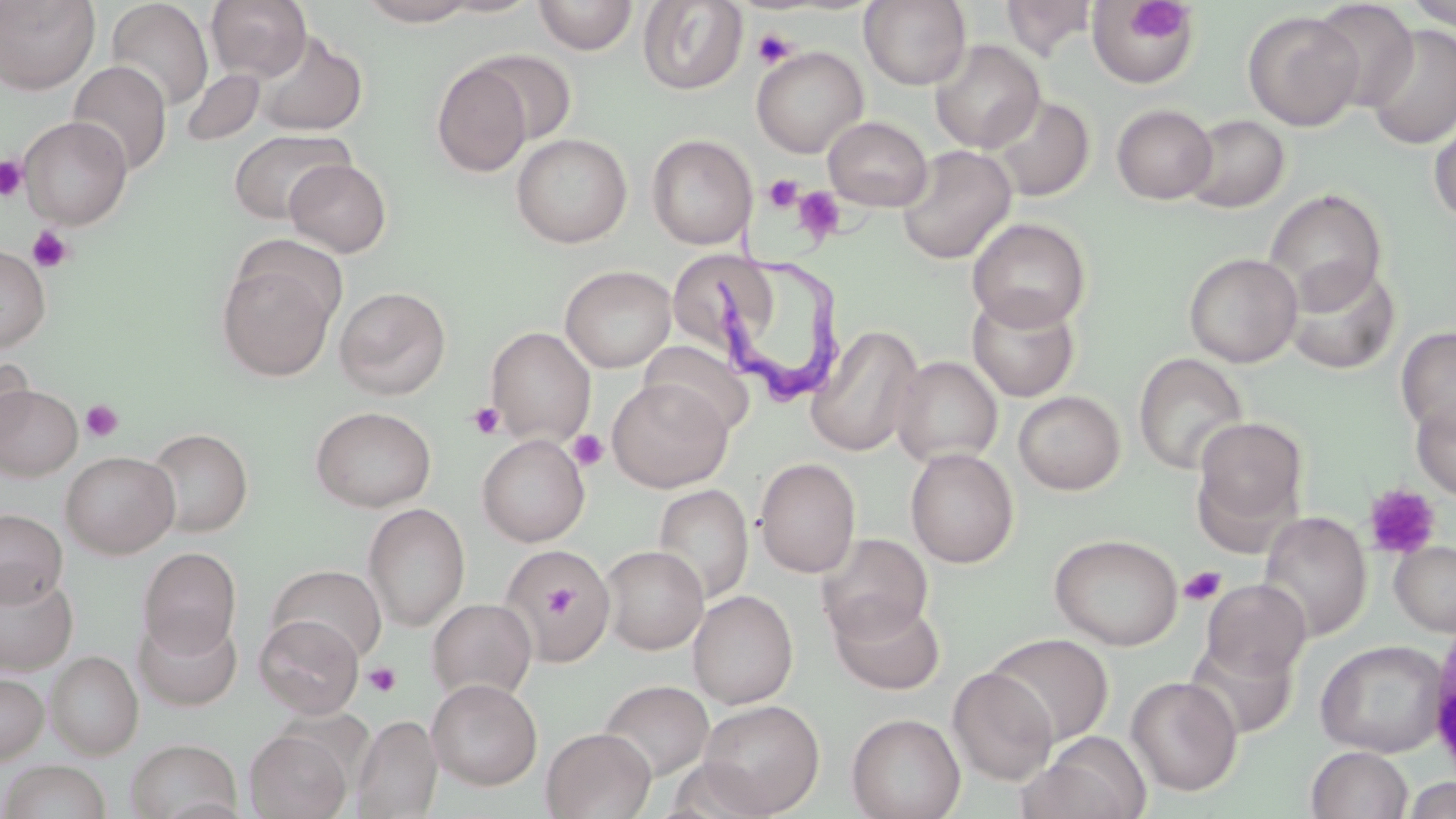

Approximate bounding boxes as (x1,y1)-(x2,y2) corner pairs in pixels. Trypanosoma brucei locations: (706,207)-(855,406). Platelet locations: (1127,4)-(1192,42), (752,28)-(798,68), (0,155)-(28,201), (763,174)-(803,212), (792,186)-(846,242), (28,225)-(74,273), (80,400)-(124,443), (468,402)-(506,440), (567,429)-(609,471), (1364,483)-(1441,559), (1179,566)-(1226,606), (539,576)-(582,627), (363,662)-(401,697). Uninfected red blood cell locations: (0,0)-(100,95), (206,0)-(312,81), (354,0)-(486,26), (533,0)-(639,55), (859,0)-(972,89), (1403,0)-(1456,31), (104,1)-(213,113), (637,1)-(747,95), (1001,1)-(1097,59), (1087,1)-(1200,89), (1310,1)-(1419,112), (1243,11)-(1363,131), (1364,24)-(1456,150), (252,29)-(368,136), (930,40)-(1045,153), (751,46)-(868,158), (469,49)-(578,145), (67,61)-(172,177), (431,63)-(533,176), (180,68)-(265,148), (987,94)-(1095,202), (1111,103)-(1218,203), (1429,111)-(1456,227), (1182,114)-(1289,213), (19,116)-(132,229), (824,116)-(933,211), (227,128)-(354,224), (511,133)-(632,248), (646,134)-(757,249), (897,145)-(1016,264), (284,158)-(392,257), (1263,188)-(1387,311), (967,217)-(1091,331), (0,244)-(51,352), (665,246)-(782,348), (1184,252)-(1302,367), (216,258)-(338,381), (1283,261)-(1400,376), (560,265)-(676,372), (334,285)-(452,399), (967,291)-(1080,402), (806,325)-(924,457), (485,326)-(596,445), (1396,326)-(1456,439), (638,340)-(755,437), (1133,352)-(1249,476), (0,355)-(34,452), (892,356)-(1003,467), (606,379)-(731,492), (0,383)-(82,481), (1013,390)-(1126,495), (1411,397)-(1456,501), (309,405)-(437,511), (1192,416)-(1308,535), (144,426)-(253,537), (477,434)-(590,546), (904,447)-(1019,568), (60,450)-(180,558), (754,457)-(861,578), (653,484)-(753,604), (362,502)-(470,632), (0,508)-(67,607), (1258,511)-(1371,642), (816,533)-(934,644), (1049,533)-(1183,650), (1390,541)-(1456,635), (499,544)-(616,663), (599,545)-(708,654), (137,547)-(241,658), (269,564)-(387,663), (0,569)-(78,675), (1202,579)-(1311,681), (688,589)-(799,709), (830,596)-(945,695), (427,597)-(537,703), (133,612)-(243,712), (254,613)-(364,718), (985,632)-(1114,746), (1315,639)-(1447,757), (46,651)-(143,759), (947,667)-(1057,785), (0,672)-(49,764), (1127,675)-(1242,796), (427,678)-(543,790), (597,680)-(713,784), (697,699)-(825,816), (846,713)-(965,819), (352,714)-(443,818), (541,727)-(656,819), (245,729)-(351,818), (1026,732)-(1152,819), (124,738)-(243,818), (1306,746)-(1413,819), (1,761)-(113,819), (1403,780)-(1454,819). Slide-level diagnosis: Trypanosoma brucei. Captured at 1000x magnification. Image is 1456×819 pixels. Thin blood film. Light microscopy. One field of a larger specimen. May-Grünwald-Giemsa stain.